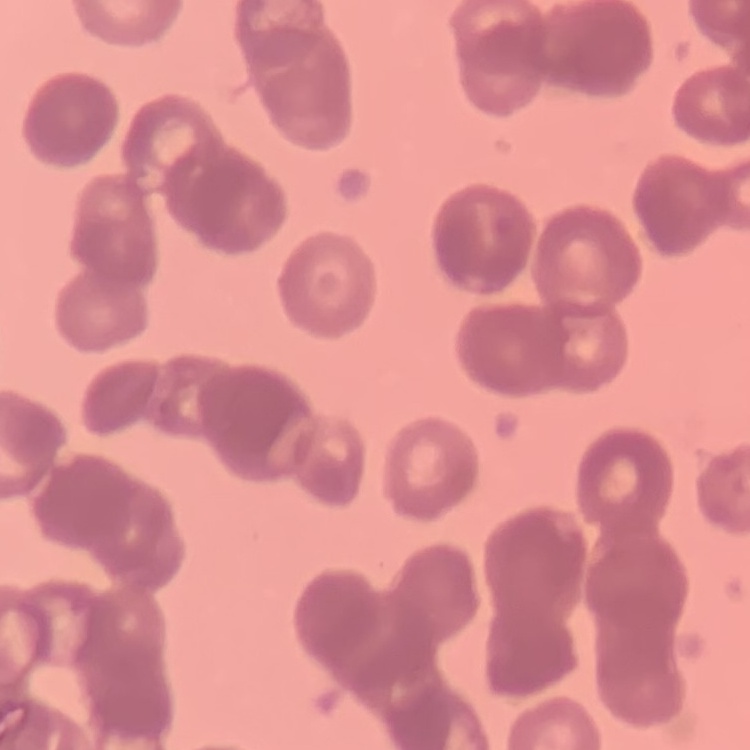
The red blood cells show rouleaux formation. Field's or Giemsa stain. Thin blood film. One tile cut from a larger photomicrograph.